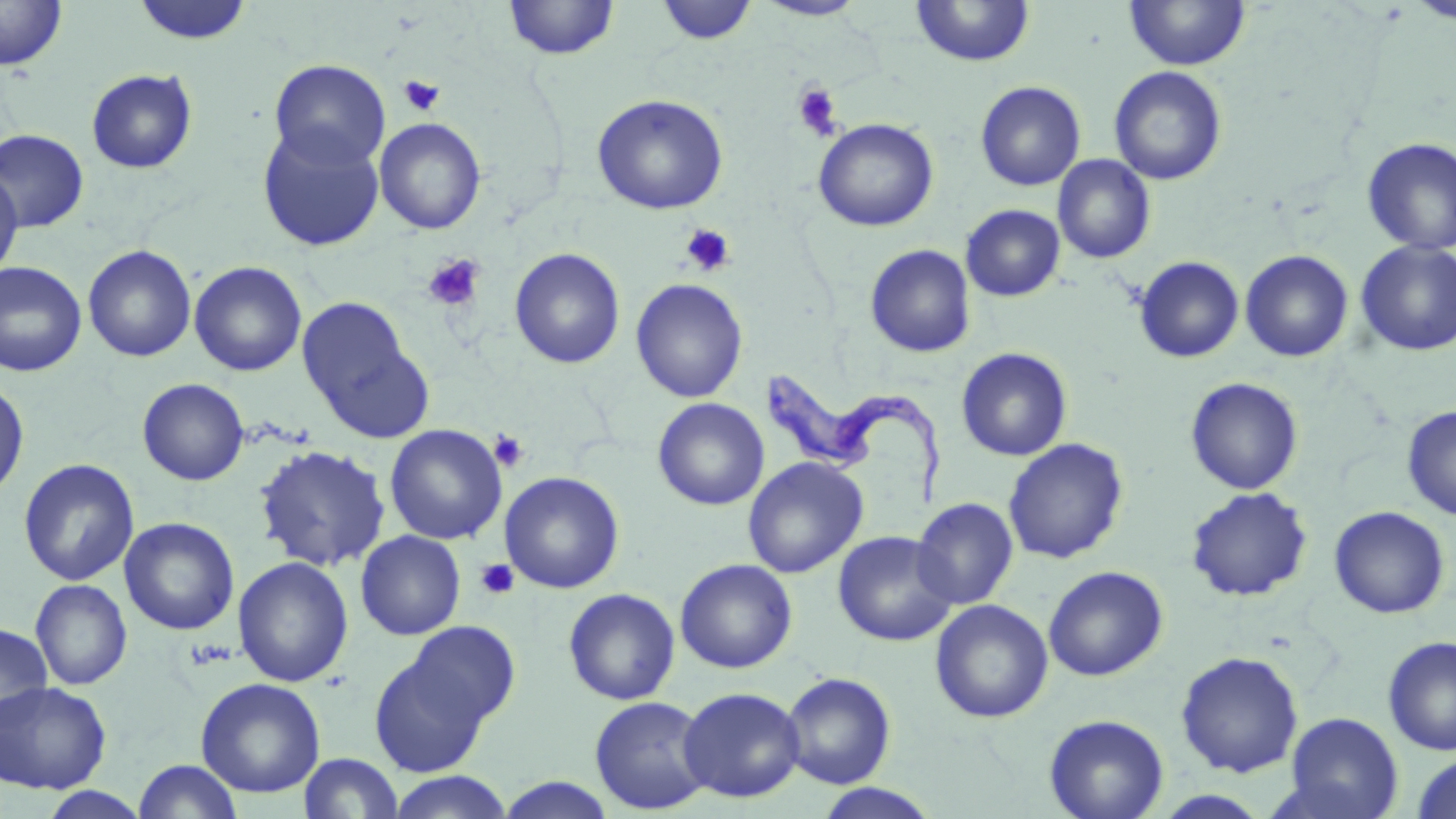
slide-level diagnosis = Trypanosoma brucei
modality = optical microscopy
uninfected red blood cell locations = approximate bounding boxes as (x1,y1)-(x2,y2) corner pairs in pixels: (504,0)-(620,60), (654,0)-(758,45), (753,0)-(868,21), (1124,0)-(1250,71), (1405,0)-(1456,26), (0,1)-(67,71), (132,1)-(255,46), (911,1)-(1035,68), (269,58)-(390,170), (1109,65)-(1227,185), (85,68)-(198,175), (975,81)-(1086,191), (591,93)-(728,214), (374,117)-(487,234), (814,118)-(938,232), (257,125)-(385,252), (0,129)-(89,232), (1361,137)-(1456,255), (1052,154)-(1156,264), (0,168)-(23,280), (961,204)-(1065,301), (1355,241)-(1456,357), (83,244)-(197,362), (865,244)-(976,358), (509,248)-(626,369), (1240,250)-(1354,362), (1134,256)-(1244,363), (0,260)-(87,377), (189,261)-(306,377), (630,278)-(748,403), (297,297)-(428,439), (956,347)-(1072,461), (1185,376)-(1303,495), (137,378)-(249,486), (0,381)-(29,501), (652,397)-(770,511), (1402,405)-(1456,521), (385,424)-(507,544), (1004,438)-(1128,564), (254,444)-(391,572), (743,456)-(868,579), (18,458)-(139,586), (500,471)-(625,594), (1185,487)-(1313,602), (912,498)-(1019,609), (1329,506)-(1450,618), (119,517)-(239,635), (355,530)-(466,640), (832,530)-(958,647), (232,556)-(354,687), (675,558)-(798,673), (1043,566)-(1169,681), (30,579)-(133,690), (563,588)-(680,705), (930,599)-(1053,724), (400,619)-(522,732), (0,623)-(53,730), (1382,635)-(1456,756), (369,644)-(496,778), (1175,650)-(1304,778), (780,672)-(896,789), (196,678)-(326,797), (0,680)-(112,793), (678,686)-(806,803), (589,696)-(713,815), (1282,712)-(1404,819), (1044,714)-(1169,819), (299,752)-(404,818), (1411,754)-(1456,819), (133,759)-(243,818), (386,771)-(514,819), (495,776)-(617,818), (813,784)-(941,818), (37,787)-(152,819), (1151,790)-(1273,818)
preparation = thin blood smear
image size = 1456×819 pixels
stain = May-Grünwald-Giemsa
magnification = 1000x
platelet locations = approximate bounding boxes as (x1,y1)-(x2,y2) corner pairs in pixels: (398,75)-(445,116), (793,83)-(843,140), (681,223)-(735,277), (422,253)-(485,312), (489,429)-(530,473), (475,558)-(519,600)
Trypanosoma brucei locations = approximate bounding boxes as (x1,y1)-(x2,y2) corner pairs in pixels: (766,368)-(945,506)
field of view = one of a larger specimen